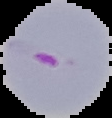
Summary:
  - Preparation: thin blood smear
  - Image size: 112×118 pixels
  - Image type: cell region segmented out of the field of view; surrounding area masked to black
  - Malaria status: parasitized